State which parasite is depicted.
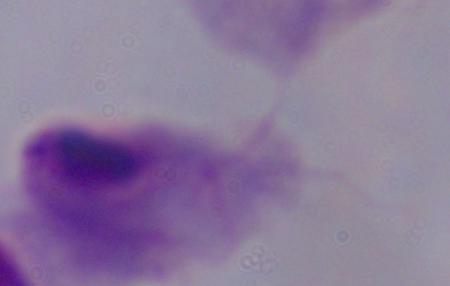
A trichomonad.

{
  "modality": "micrograph",
  "magnification": "1000x"
}